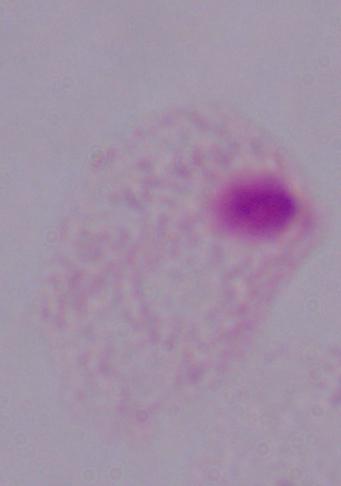

Summary:
  - Identification: trichomonad
  - Magnification: 1000x
  - Modality: micrograph